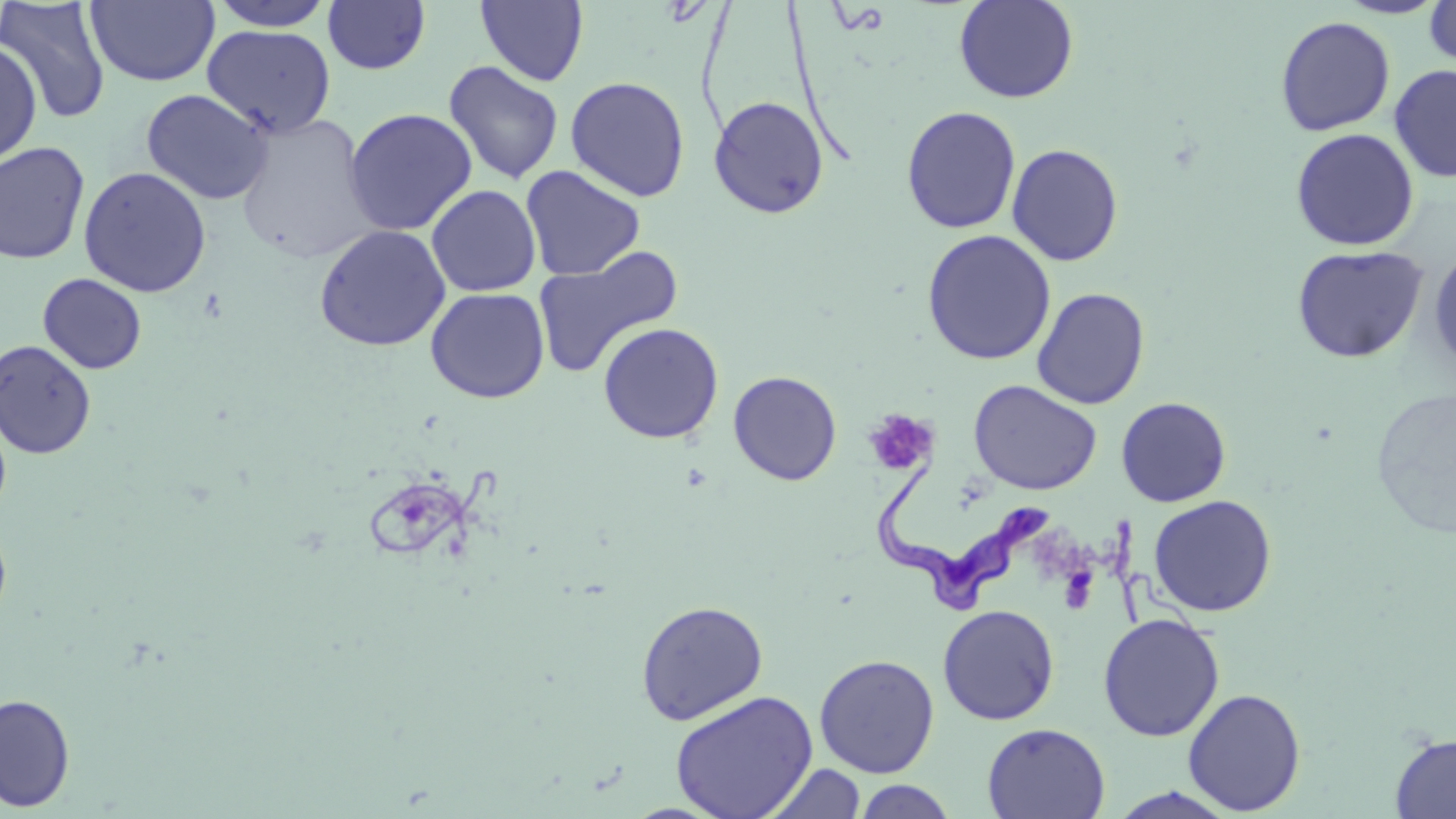

trypanosoma_brucei_locations: 'approximate bounding boxes as (x1, y1, x2, y2) in pixels: (873, 467, 1053, 614)'
slide_level_diagnosis: Trypanosoma brucei
preparation: thin blood film
field_of_view: one of a larger specimen
stain: May-Grünwald-Giemsa
modality: light microscopy
platelet_locations: 'approximate bounding boxes as (x1, y1, x2, y2) in pixels: (863, 409, 938, 477), (1058, 566, 1099, 614)'
magnification: 1000x
image_size: 1456×819 pixels
uninfected_red_blood_cell_locations: 'approximate bounding boxes as (x1, y1, x2, y2) in pixels: (207, 0, 336, 31), (954, 0, 1078, 104), (1333, 0, 1451, 19), (1424, 0, 1456, 69), (0, 1, 111, 124), (86, 1, 220, 87), (323, 1, 431, 75), (476, 1, 588, 86), (1275, 16, 1395, 136), (202, 24, 337, 139), (0, 41, 42, 167), (443, 60, 564, 185), (1389, 64, 1456, 183), (565, 76, 690, 201), (141, 88, 273, 205), (708, 96, 830, 219), (901, 106, 1021, 234), (344, 108, 478, 236), (235, 114, 377, 264), (1290, 128, 1419, 251), (0, 142, 90, 265), (1006, 143, 1124, 267), (521, 165, 645, 281), (78, 166, 212, 297), (427, 185, 541, 297), (313, 224, 451, 351), (921, 230, 1056, 365), (1291, 244, 1429, 363), (533, 245, 684, 378), (1428, 247, 1456, 372), (37, 273, 147, 374), (425, 286, 550, 404), (1031, 287, 1150, 409), (598, 322, 724, 444), (0, 339, 97, 459), (728, 370, 842, 485), (968, 380, 1103, 496), (1370, 386, 1456, 540), (1116, 396, 1231, 507), (0, 407, 12, 524), (1148, 494, 1277, 617), (0, 518, 12, 630), (635, 600, 768, 725), (937, 604, 1060, 725), (1097, 613, 1225, 742), (813, 654, 940, 778), (962, 658, 1082, 812), (1182, 688, 1306, 815), (668, 690, 818, 819), (0, 693, 75, 812), (981, 722, 1110, 819), (1390, 733, 1456, 818), (760, 763, 867, 819), (852, 778, 958, 818), (1106, 787, 1241, 819)'